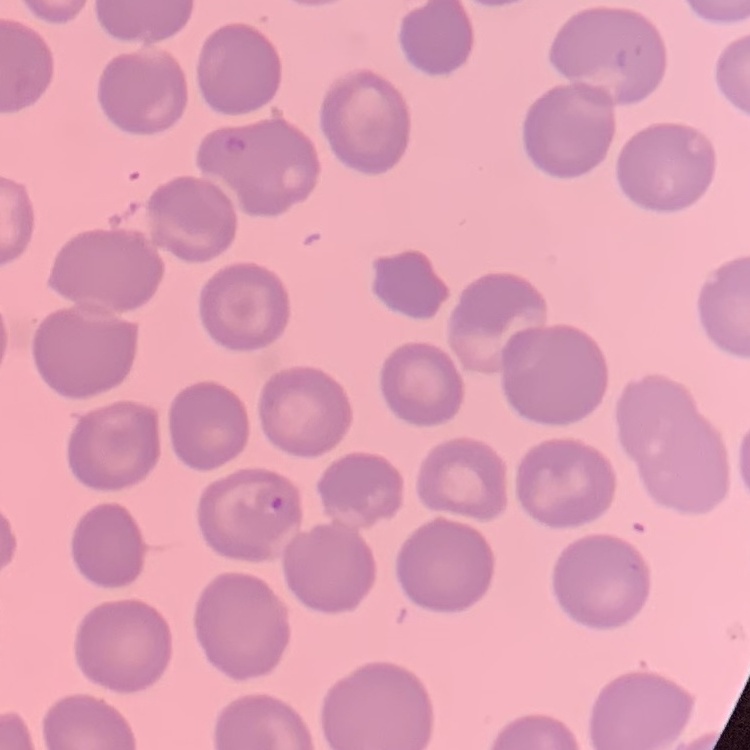 The red blood cells show no rouleaux formation. Stained with either Field's or Giemsa. Square crop of a larger photomicrograph. Thin blood film.